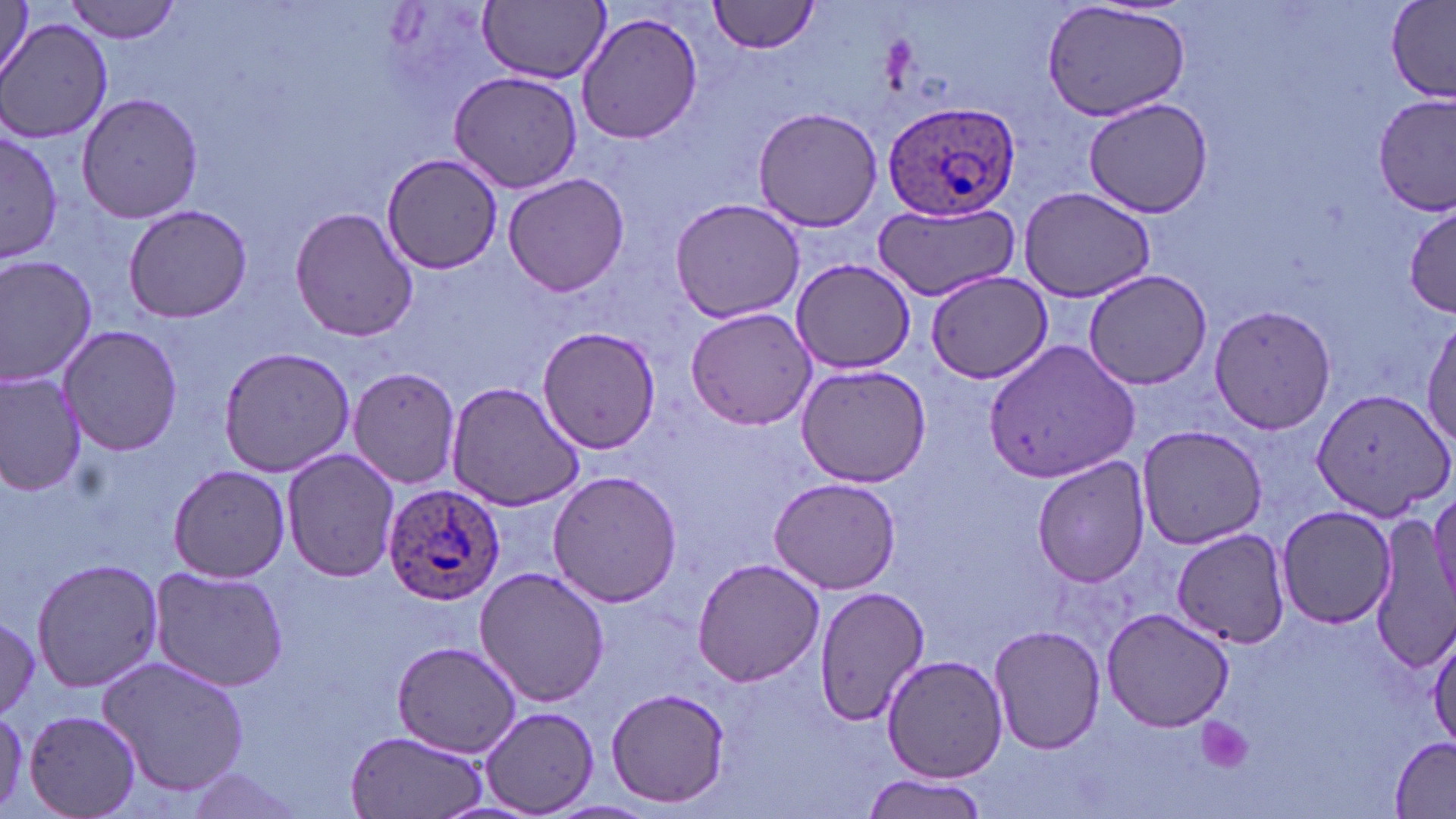
Approximate bounding boxes as (x1,y1)-(x2,y2) corner pairs in pixels. Uninfected red blood cell locations: (61,0)-(185,43), (709,0)-(823,54), (1386,0)-(1456,102), (478,1)-(610,83), (1042,1)-(1191,122), (1,2)-(37,81), (576,11)-(704,146), (4,18)-(114,145), (447,69)-(584,193), (76,92)-(203,225), (1374,96)-(1453,216), (1082,97)-(1212,217), (752,104)-(883,233), (0,127)-(61,266), (380,153)-(504,276), (502,172)-(632,296), (1018,187)-(1156,301), (669,195)-(808,323), (871,199)-(1021,302), (1405,202)-(1456,316), (122,204)-(253,323), (291,204)-(417,343), (0,253)-(99,387), (791,257)-(917,374), (1083,270)-(1214,390), (926,271)-(1054,384), (1207,303)-(1337,434), (684,305)-(817,429), (1418,318)-(1455,453), (57,323)-(184,456), (535,326)-(662,454), (986,340)-(1140,485), (216,346)-(357,478), (795,360)-(930,489), (347,366)-(463,491), (0,370)-(89,496), (444,380)-(586,511), (1311,385)-(1454,521), (1134,423)-(1268,551), (280,449)-(402,582), (1032,456)-(1152,588), (166,464)-(293,584), (546,468)-(683,608), (769,476)-(902,595), (1428,485)-(1456,607), (1277,506)-(1399,630), (1370,521)-(1456,671), (1170,526)-(1290,649), (31,556)-(163,693), (690,558)-(824,686), (148,566)-(293,695), (474,566)-(610,707), (813,586)-(930,726), (1101,607)-(1236,732), (0,612)-(42,722), (988,623)-(1106,755), (1428,624)-(1456,751), (390,641)-(521,758), (96,653)-(251,798), (881,653)-(1008,782), (606,686)-(734,808), (482,706)-(600,818), (23,708)-(143,819), (343,728)-(491,819), (1389,737)-(1455,815), (177,764)-(310,815), (860,774)-(989,817). Plasmodium ovale-infected red blood cell locations: (883,99)-(1021,220), (381,482)-(506,608). Platelet locations: (1196,718)-(1253,775). Slide-level diagnosis: Plasmodium ovale. May-Grünwald-Giemsa-stained preparation. Thin blood film. Captured at 1000x magnification. Light microscopy. Single field of view. Image is 1456×819 pixels.